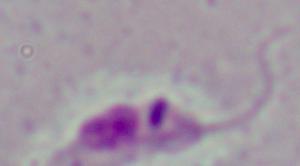

Summary:
  - Identification: Leishmania
  - Modality: micrograph
  - Magnification: 1000x